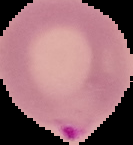
image type = segmented cell region on a black background
preparation = thin blood smear
malaria status = parasitized
image size = 133×145 pixels